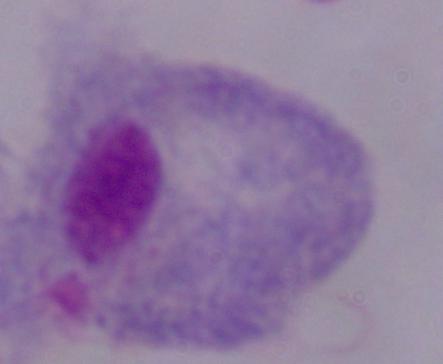 A trichomonad is shown. 1000x magnification. Micrograph.